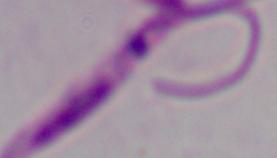
{
  "modality": "micrograph",
  "identification": "Leishmania",
  "magnification": "1000x"
}